Give the extent of all uninfected red blood cells.
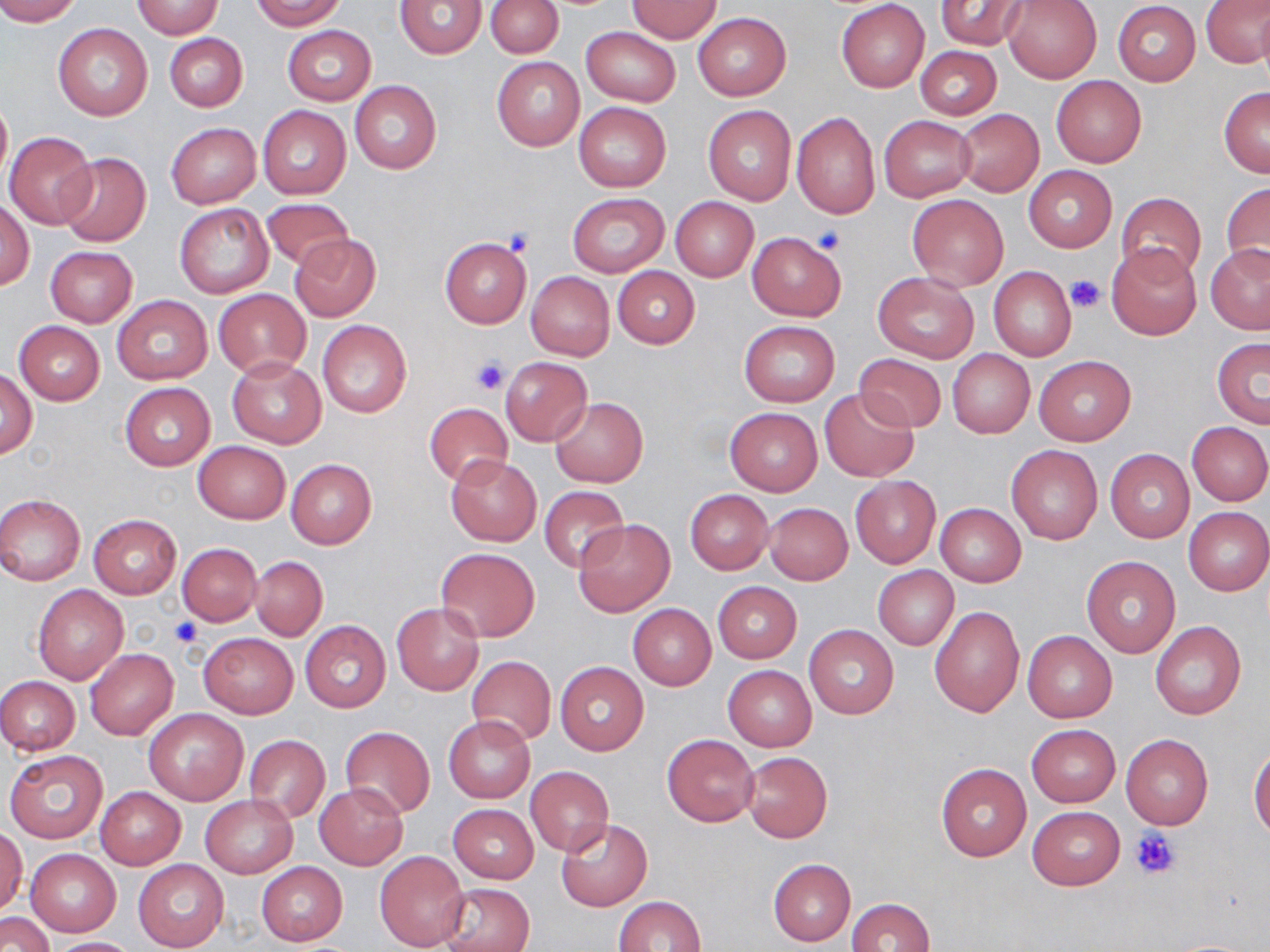
Approximate bounding boxes as (x1, y1, x2, y2) in pixels.
Uninfected red blood cells: (0, 0, 80, 25), (250, 0, 346, 30), (487, 0, 563, 58), (836, 0, 930, 93), (1003, 0, 1102, 83), (1202, 0, 1270, 69), (132, 1, 223, 39), (395, 1, 486, 59), (625, 1, 723, 43), (935, 1, 1031, 50), (1112, 2, 1201, 86), (693, 11, 791, 101), (51, 21, 153, 121), (283, 25, 375, 104), (582, 27, 680, 106), (163, 32, 248, 112), (915, 46, 1001, 120), (492, 56, 585, 152), (1052, 75, 1146, 167), (349, 81, 441, 173), (1219, 86, 1270, 176), (0, 95, 11, 189), (573, 102, 671, 192), (703, 105, 796, 205), (258, 106, 351, 199), (954, 109, 1044, 197), (790, 111, 880, 219), (878, 115, 974, 201), (166, 123, 261, 207), (4, 130, 98, 229), (55, 151, 152, 247), (1024, 166, 1116, 253), (1222, 182, 1270, 274), (1116, 192, 1206, 282), (568, 193, 669, 277), (907, 194, 1008, 290), (670, 197, 758, 281), (1, 198, 35, 290), (260, 198, 355, 271), (175, 204, 273, 298), (747, 232, 846, 320), (290, 234, 381, 323), (439, 238, 531, 328), (1106, 242, 1203, 340), (1205, 244, 1270, 335), (46, 247, 137, 327), (613, 266, 700, 348), (989, 268, 1077, 361), (526, 271, 615, 360), (872, 271, 979, 362), (212, 288, 312, 377), (111, 295, 212, 385), (317, 320, 411, 418), (14, 321, 105, 405), (740, 322, 840, 406), (1212, 337, 1270, 429), (947, 349, 1035, 439), (854, 353, 948, 433), (226, 355, 327, 448), (1032, 355, 1136, 446), (500, 357, 592, 446), (0, 370, 37, 459), (119, 383, 216, 470), (819, 386, 918, 482), (549, 397, 648, 487), (423, 403, 514, 487), (726, 407, 822, 496), (1187, 421, 1269, 507), (193, 441, 290, 523), (1005, 445, 1103, 544), (1106, 449, 1194, 542), (446, 455, 541, 546), (285, 459, 377, 548), (850, 476, 940, 568), (540, 486, 629, 572), (684, 490, 774, 575), (0, 494, 86, 585), (762, 502, 853, 584), (935, 503, 1026, 586), (1183, 507, 1270, 595), (87, 515, 182, 600), (573, 519, 676, 617), (178, 543, 261, 626), (437, 547, 540, 642), (251, 556, 327, 640), (1080, 556, 1181, 659), (874, 566, 959, 650), (713, 582, 802, 663), (32, 584, 129, 683), (628, 603, 716, 690), (392, 604, 485, 695), (930, 605, 1024, 717), (1150, 620, 1248, 720), (299, 621, 391, 713), (804, 624, 899, 719), (1023, 630, 1117, 723), (199, 632, 297, 718), (85, 648, 177, 739), (467, 656, 556, 747), (555, 661, 650, 756), (723, 665, 816, 751), (0, 676, 80, 755), (144, 708, 249, 805), (444, 716, 535, 802), (1027, 724, 1120, 807), (339, 726, 434, 820), (662, 734, 759, 826), (1120, 734, 1213, 829), (246, 735, 329, 823), (1249, 747, 1270, 840), (6, 750, 108, 845), (741, 751, 833, 843), (935, 762, 1031, 862), (526, 767, 613, 855), (315, 783, 408, 868), (96, 786, 185, 869), (201, 795, 297, 878), (448, 804, 538, 884), (1027, 807, 1124, 890), (555, 818, 652, 912), (0, 827, 26, 915), (26, 849, 121, 937), (375, 852, 470, 951), (133, 859, 229, 952), (768, 859, 855, 946), (256, 861, 348, 945), (440, 882, 534, 952), (614, 896, 707, 951), (848, 898, 935, 952), (3, 912, 53, 952), (47, 937, 140, 951).

Platelet locations: (815, 226, 846, 254), (504, 228, 536, 256), (1065, 274, 1105, 312), (469, 355, 510, 395), (171, 617, 202, 647), (1131, 827, 1180, 879). Slide-level diagnosis: no evidence of blood parasites. May-Grünwald-Giemsa stain. 1000x magnification. Thin blood film. Image is 1270×952 pixels. Single field of view. Light microscopy.